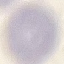

result = negative for malaria parasites
stain = Giemsa
image type = automatically extracted cell patch, resized to 64 × 64 pixels
preparation = thin blood smear
capture = smartphone through the microscope eyepiece